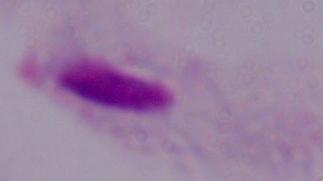
modality = micrograph
identification = trichomonad
magnification = 1000x